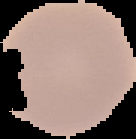 Image is 136×139 pixels. Malaria status: uninfected. Segmented cell region on a black background. From a thin blood smear.